Locate and identify every blood parasite.
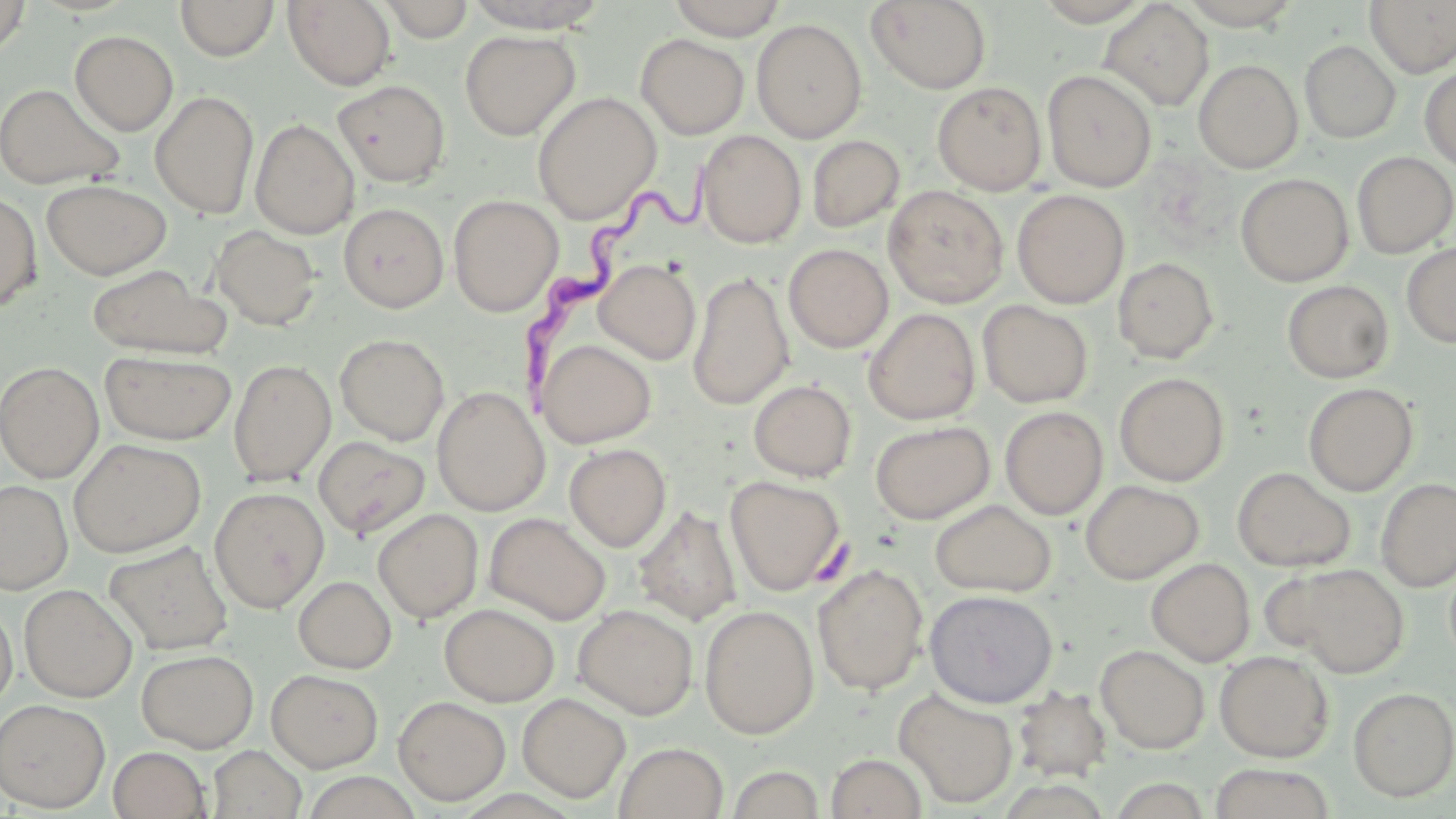
Approximate bounding boxes as named x1/y1/x2/y2 corners in pixels.
Trypanosoma brucei: (x1=519, y1=166, x2=724, y2=399).
No Plasmodium falciparum, Plasmodium ovale, Plasmodium malariae, Plasmodium vivax, or Babesia divergens observed.

Uninfected red blood cell locations: (x1=0, y1=0, x2=31, y2=58), (x1=176, y1=0, x2=279, y2=61), (x1=283, y1=0, x2=396, y2=90), (x1=378, y1=0, x2=477, y2=42), (x1=462, y1=0, x2=611, y2=33), (x1=667, y1=0, x2=788, y2=40), (x1=1031, y1=0, x2=1156, y2=26), (x1=1176, y1=0, x2=1304, y2=29), (x1=866, y1=1, x2=991, y2=94), (x1=1099, y1=1, x2=1214, y2=110), (x1=1365, y1=1, x2=1456, y2=77), (x1=751, y1=18, x2=867, y2=143), (x1=70, y1=30, x2=178, y2=136), (x1=460, y1=30, x2=579, y2=140), (x1=635, y1=34, x2=749, y2=139), (x1=1300, y1=40, x2=1401, y2=143), (x1=1194, y1=59, x2=1303, y2=173), (x1=1420, y1=66, x2=1456, y2=172), (x1=1042, y1=69, x2=1157, y2=192), (x1=333, y1=79, x2=450, y2=187), (x1=932, y1=81, x2=1047, y2=195), (x1=0, y1=83, x2=124, y2=190), (x1=150, y1=90, x2=259, y2=217), (x1=532, y1=92, x2=661, y2=223), (x1=251, y1=118, x2=359, y2=238), (x1=696, y1=130, x2=806, y2=248), (x1=807, y1=135, x2=905, y2=233), (x1=1352, y1=152, x2=1456, y2=257), (x1=1236, y1=173, x2=1354, y2=286), (x1=41, y1=179, x2=171, y2=279), (x1=884, y1=186, x2=1008, y2=307), (x1=1012, y1=189, x2=1129, y2=308), (x1=0, y1=191, x2=42, y2=313), (x1=448, y1=194, x2=563, y2=316), (x1=338, y1=203, x2=449, y2=312), (x1=211, y1=225, x2=322, y2=330), (x1=1401, y1=242, x2=1456, y2=348), (x1=784, y1=243, x2=893, y2=352), (x1=1113, y1=257, x2=1218, y2=363), (x1=595, y1=259, x2=700, y2=364), (x1=86, y1=264, x2=230, y2=359), (x1=688, y1=271, x2=794, y2=409), (x1=1283, y1=280, x2=1394, y2=383), (x1=978, y1=300, x2=1093, y2=408), (x1=864, y1=309, x2=980, y2=425), (x1=335, y1=334, x2=449, y2=445), (x1=537, y1=338, x2=656, y2=448), (x1=554, y1=338, x2=663, y2=553), (x1=99, y1=351, x2=237, y2=444), (x1=228, y1=359, x2=336, y2=485), (x1=0, y1=361, x2=104, y2=482), (x1=1114, y1=372, x2=1230, y2=486), (x1=749, y1=380, x2=857, y2=482), (x1=1304, y1=383, x2=1418, y2=495), (x1=432, y1=386, x2=549, y2=516), (x1=1000, y1=406, x2=1108, y2=519), (x1=870, y1=421, x2=994, y2=524), (x1=313, y1=436, x2=430, y2=539), (x1=69, y1=438, x2=206, y2=557), (x1=564, y1=443, x2=671, y2=551), (x1=1232, y1=467, x2=1356, y2=571), (x1=725, y1=475, x2=847, y2=596), (x1=1376, y1=477, x2=1456, y2=591), (x1=0, y1=480, x2=73, y2=593), (x1=1080, y1=480, x2=1204, y2=584), (x1=209, y1=487, x2=329, y2=612), (x1=930, y1=499, x2=1056, y2=597), (x1=633, y1=505, x2=742, y2=626), (x1=373, y1=508, x2=484, y2=623), (x1=485, y1=513, x2=611, y2=624), (x1=103, y1=541, x2=233, y2=654), (x1=1146, y1=558, x2=1255, y2=666), (x1=1444, y1=558, x2=1456, y2=667), (x1=1276, y1=563, x2=1410, y2=677), (x1=812, y1=564, x2=929, y2=695), (x1=293, y1=575, x2=396, y2=673), (x1=19, y1=583, x2=137, y2=702), (x1=924, y1=589, x2=1058, y2=707), (x1=0, y1=603, x2=17, y2=710), (x1=439, y1=603, x2=560, y2=706), (x1=699, y1=604, x2=820, y2=738), (x1=573, y1=605, x2=698, y2=719), (x1=1095, y1=644, x2=1210, y2=754), (x1=136, y1=648, x2=258, y2=752), (x1=1214, y1=650, x2=1334, y2=762), (x1=266, y1=668, x2=383, y2=771), (x1=1012, y1=686, x2=1112, y2=781), (x1=1348, y1=686, x2=1456, y2=801), (x1=894, y1=688, x2=1018, y2=808), (x1=517, y1=693, x2=631, y2=803), (x1=393, y1=695, x2=511, y2=805), (x1=0, y1=699, x2=111, y2=812), (x1=614, y1=742, x2=728, y2=819), (x1=206, y1=744, x2=307, y2=818), (x1=107, y1=746, x2=212, y2=818), (x1=825, y1=752, x2=928, y2=819), (x1=1208, y1=763, x2=1336, y2=819), (x1=725, y1=765, x2=826, y2=819). Slide-level diagnosis: Trypanosoma brucei. Image is 1456×819 pixels. Light microscopy. May-Grünwald-Giemsa-stained preparation. Single field of view. Captured at 1000x magnification. Thin blood film.